Give the extent of all Plasmodium falciparum-infected red blood cells.
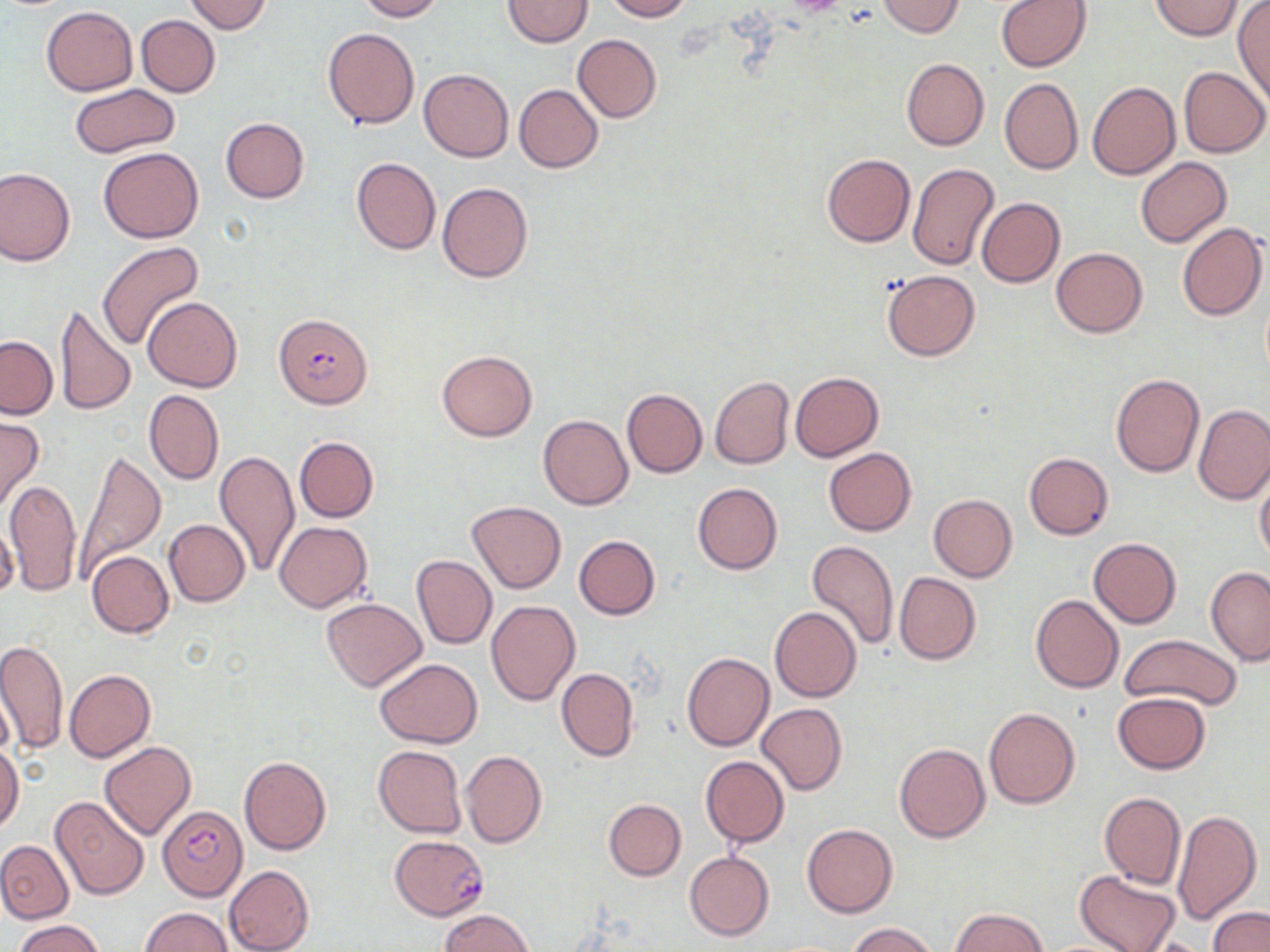
Approximate bounding boxes as [x1, y1, x2, y2] in pixels.
Plasmodium falciparum-infected red blood cells: [273, 312, 372, 408], [157, 805, 247, 900], [390, 835, 489, 920].

{
  "slide_level_diagnosis": "Plasmodium falciparum",
  "stain": "May-Grünwald-Giemsa",
  "magnification": "1000x",
  "modality": "optical microscopy",
  "field_of_view": "one of a larger specimen",
  "uninfected_red_blood_cell_locations": "approximate bounding boxes as [x1, y1, x2, y2] in pixels: [182, 0, 273, 34], [356, 0, 444, 21], [503, 0, 592, 47], [600, 0, 691, 21], [875, 0, 965, 37], [1151, 0, 1243, 40], [994, 1, 1092, 72], [1232, 1, 1270, 106], [42, 7, 138, 95], [137, 14, 220, 97], [322, 27, 419, 128], [572, 34, 662, 122], [900, 57, 989, 151], [1179, 66, 1269, 157], [419, 69, 514, 162], [999, 78, 1083, 174], [1088, 82, 1180, 181], [68, 84, 179, 158], [514, 84, 604, 172], [220, 118, 309, 202], [99, 146, 204, 243], [821, 153, 915, 247], [351, 157, 441, 255], [1135, 157, 1232, 247], [906, 162, 999, 270], [0, 167, 75, 266], [436, 181, 533, 282], [977, 198, 1065, 287], [1177, 222, 1268, 321], [95, 241, 202, 351], [1051, 247, 1148, 337], [881, 270, 980, 360], [143, 297, 243, 392], [57, 303, 135, 417], [0, 336, 57, 418], [436, 349, 537, 441], [790, 372, 883, 461], [1110, 372, 1205, 477], [709, 376, 794, 470], [622, 389, 707, 478], [144, 390, 224, 485], [1193, 405, 1270, 504], [0, 415, 44, 514], [538, 415, 633, 510], [294, 436, 379, 521], [74, 447, 164, 576], [823, 448, 916, 536], [215, 451, 300, 579], [1024, 452, 1113, 540], [1255, 470, 1270, 568], [5, 477, 82, 597], [692, 482, 782, 574], [928, 493, 1017, 581], [467, 501, 566, 594], [163, 519, 250, 606], [275, 521, 372, 612], [573, 535, 659, 620], [1088, 537, 1181, 628], [807, 540, 899, 651], [87, 551, 174, 638], [411, 555, 496, 649], [1205, 566, 1270, 663], [893, 572, 981, 665], [1030, 594, 1123, 693], [321, 597, 428, 692], [486, 600, 581, 707], [770, 606, 861, 702], [1120, 634, 1242, 714], [0, 638, 67, 756], [682, 651, 774, 752], [375, 658, 481, 747], [557, 667, 639, 761], [65, 669, 155, 762], [1112, 692, 1210, 773], [756, 704, 847, 795], [983, 707, 1080, 808], [100, 741, 196, 840], [894, 743, 990, 843], [0, 744, 23, 834], [373, 745, 466, 837], [459, 749, 547, 849], [239, 754, 332, 854], [700, 755, 789, 847], [1099, 792, 1186, 888], [51, 795, 150, 900], [603, 798, 686, 881], [1172, 809, 1262, 925], [802, 823, 897, 917], [0, 840, 73, 923], [685, 850, 775, 941], [224, 865, 315, 952], [1075, 870, 1181, 952], [1207, 906, 1270, 952], [138, 907, 232, 951], [949, 908, 1049, 952], [441, 910, 532, 952], [13, 919, 106, 952], [848, 922, 936, 952], [1133, 936, 1217, 952]",
  "image_size": "1270×952 pixels",
  "preparation": "thin blood smear"
}